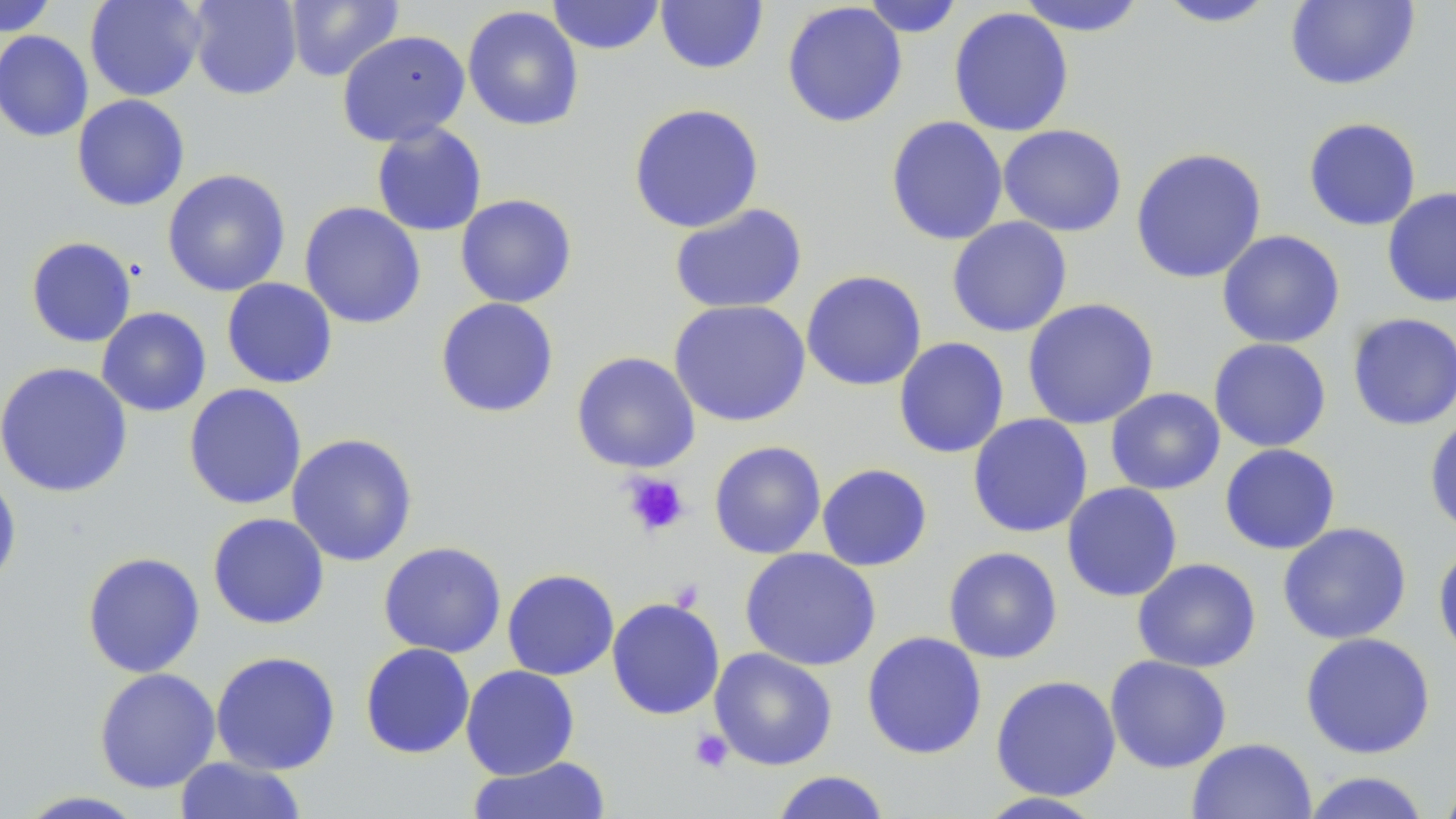

slide-level diagnosis = negative for blood parasites
preparation = thin blood smear
image size = 1456×819 pixels
magnification = 1000x
platelet locations = approximate bounding boxes as [x1, y1, x2, y2] in pixels: [622, 472, 690, 538], [689, 728, 734, 773]
stain = May-Grünwald-Giemsa
modality = optical microscopy
uninfected red blood cell locations = approximate bounding boxes as [x1, y1, x2, y2] in pixels: [0, 0, 59, 36], [84, 0, 207, 101], [187, 0, 302, 100], [285, 0, 405, 83], [547, 0, 666, 55], [655, 0, 769, 74], [861, 0, 964, 37], [1015, 0, 1148, 37], [1155, 1, 1280, 28], [1285, 1, 1421, 91], [782, 2, 908, 128], [462, 5, 584, 131], [948, 7, 1075, 137], [0, 30, 93, 142], [337, 30, 471, 147], [71, 94, 190, 211], [627, 102, 765, 233], [885, 116, 1008, 246], [1303, 117, 1422, 231], [371, 122, 488, 237], [998, 124, 1127, 237], [1130, 147, 1267, 284], [162, 168, 291, 297], [1381, 188, 1456, 307], [454, 193, 578, 308], [299, 201, 427, 329], [669, 203, 807, 315], [946, 216, 1072, 337], [1216, 229, 1345, 349], [25, 236, 138, 348], [801, 270, 927, 391], [222, 277, 338, 389], [434, 297, 560, 419], [1022, 298, 1159, 430], [668, 300, 812, 427], [96, 307, 211, 417], [1347, 312, 1456, 431], [893, 337, 1010, 459], [1208, 338, 1332, 452], [571, 351, 701, 473], [0, 362, 133, 498], [183, 383, 307, 510], [1105, 387, 1225, 495], [967, 413, 1093, 538], [1424, 416, 1456, 538], [286, 432, 418, 567], [709, 441, 826, 560], [1219, 443, 1341, 554], [817, 463, 933, 571], [0, 469, 22, 591], [1061, 482, 1183, 602], [207, 512, 330, 630], [1277, 522, 1412, 645], [378, 541, 507, 658], [1432, 541, 1456, 662], [943, 546, 1063, 664], [739, 547, 881, 671], [81, 551, 205, 678], [1132, 558, 1261, 673], [502, 568, 619, 680], [606, 596, 725, 720], [861, 631, 987, 760], [1300, 631, 1436, 759], [359, 642, 475, 759], [709, 648, 838, 770], [210, 650, 341, 775], [1104, 654, 1232, 774], [461, 665, 580, 779], [94, 667, 221, 793], [990, 675, 1121, 801], [1187, 738, 1317, 819], [173, 756, 308, 818], [467, 756, 613, 819], [769, 770, 892, 819], [1437, 770, 1456, 819], [1301, 771, 1432, 819], [13, 790, 149, 818], [973, 792, 1109, 818]
field of view = one of a larger specimen